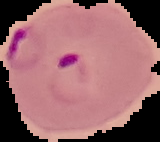

From a thin blood smear. Image is 160×142 pixels. Result: malaria parasites detected. The area outside the segmented cell region is set to black.